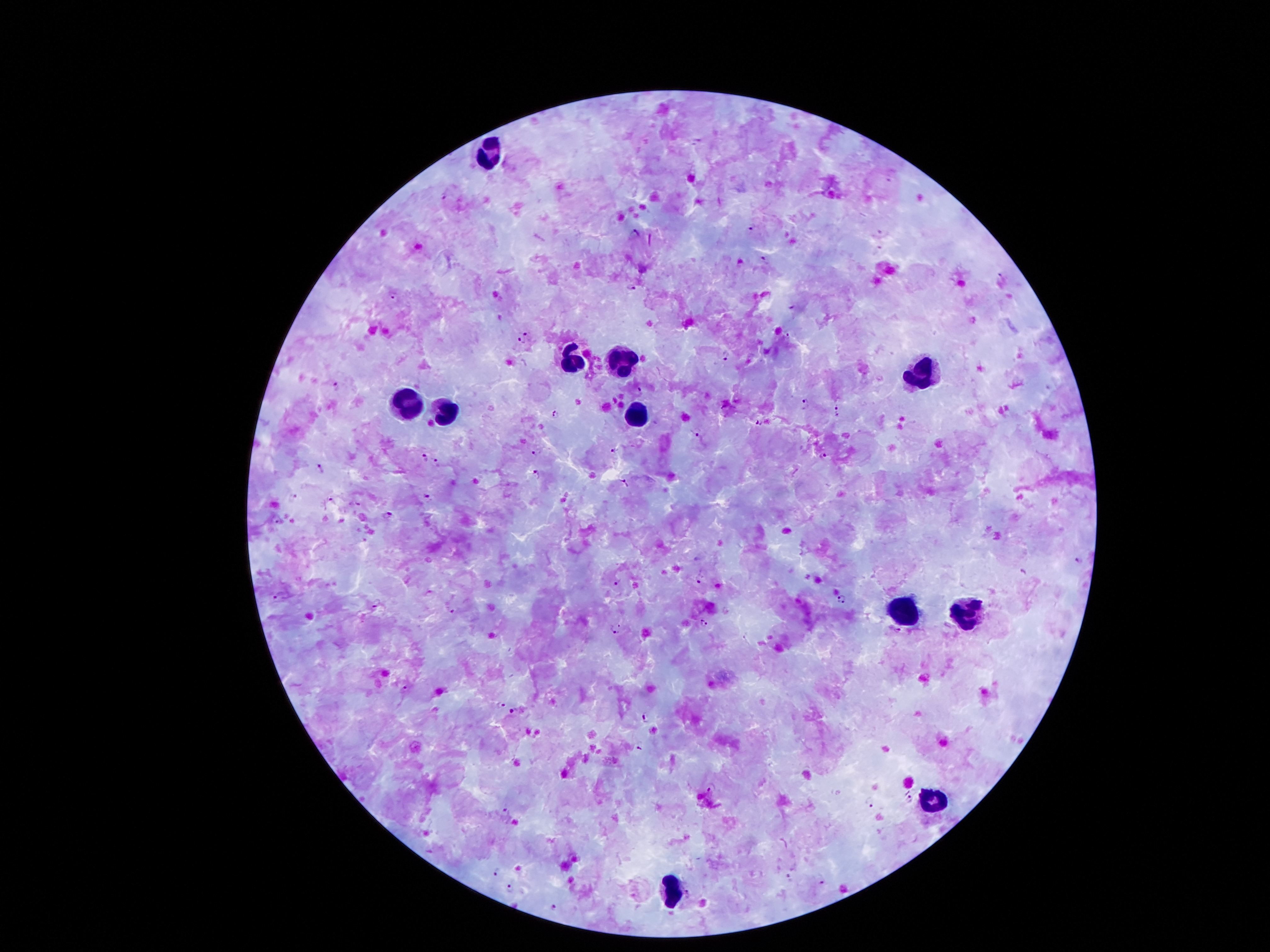
Approximate centers as (x, y) in pixels.
Summary:
  - Leukocyte locations: (491, 151), (621, 360), (576, 364), (924, 375), (442, 403), (406, 407), (640, 414), (969, 612), (901, 614), (933, 804), (673, 890)
  - Malaria parasite locations: (892, 175), (446, 193), (753, 229), (636, 233), (879, 233), (879, 247), (763, 261), (1002, 279), (632, 287), (393, 294), (794, 308), (526, 335), (520, 341), (724, 357), (334, 383), (1049, 387), (638, 392), (805, 405), (838, 410), (557, 414), (759, 424), (698, 432), (610, 450), (536, 451), (823, 455), (422, 456), (438, 461), (321, 470), (536, 473), (627, 484), (428, 494), (293, 497), (330, 499), (357, 503), (389, 515), (278, 520), (1078, 562), (1024, 570), (699, 579), (618, 582), (277, 593), (841, 598), (377, 604), (451, 611), (703, 624), (617, 628), (403, 689), (501, 705), (515, 710), (646, 718), (638, 749), (711, 789), (908, 800), (870, 802), (507, 810), (496, 871), (790, 877), (822, 882), (511, 889), (688, 894), (554, 906)
  - Image size: 1270×952 pixels
  - Magnification: 100x
  - Preparation: thick peripheral-blood smear
  - Stain: Giemsa
  - Patient malaria status: positive for Plasmodium falciparum
  - Field of view: single
  - Capture: smartphone through the microscope eyepiece